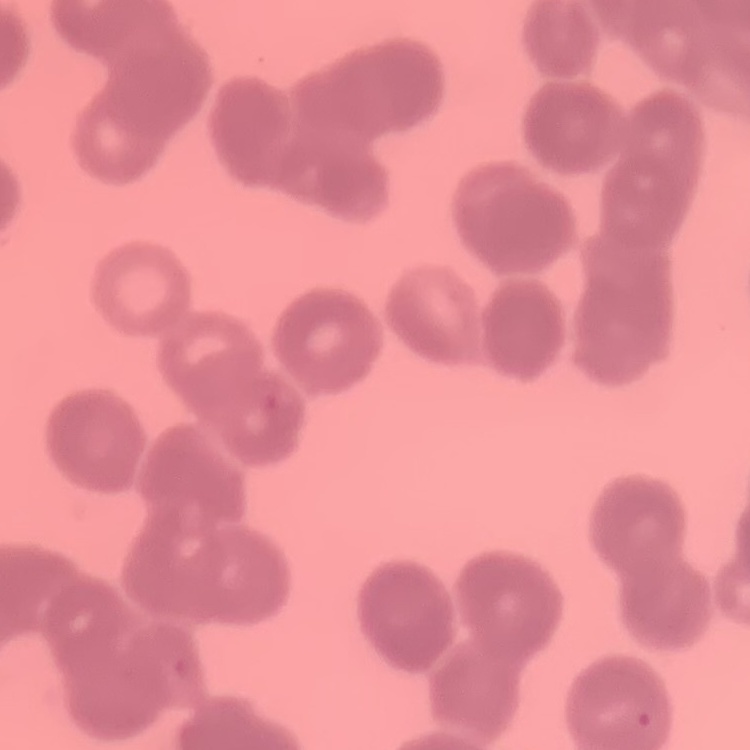 The red blood cells show rouleaux formation. Square crop of a larger photomicrograph. Field's or Giemsa stain. Thin peripheral smear.